Identify the cell.
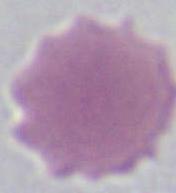

This is an erythrocyte.

1000x magnification. Photomicrograph.